Identify the cell.
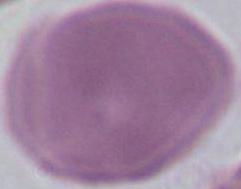

This is an erythrocyte.

Photomicrograph. 1000x magnification.